Assess this cell for malaria.
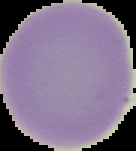

It is uninfected.

Summary:
  - Preparation: thin blood smear
  - Image type: segmented cell region with the area outside set to black
  - Image size: 136×151 pixels